Locate every uninfected red blood cell.
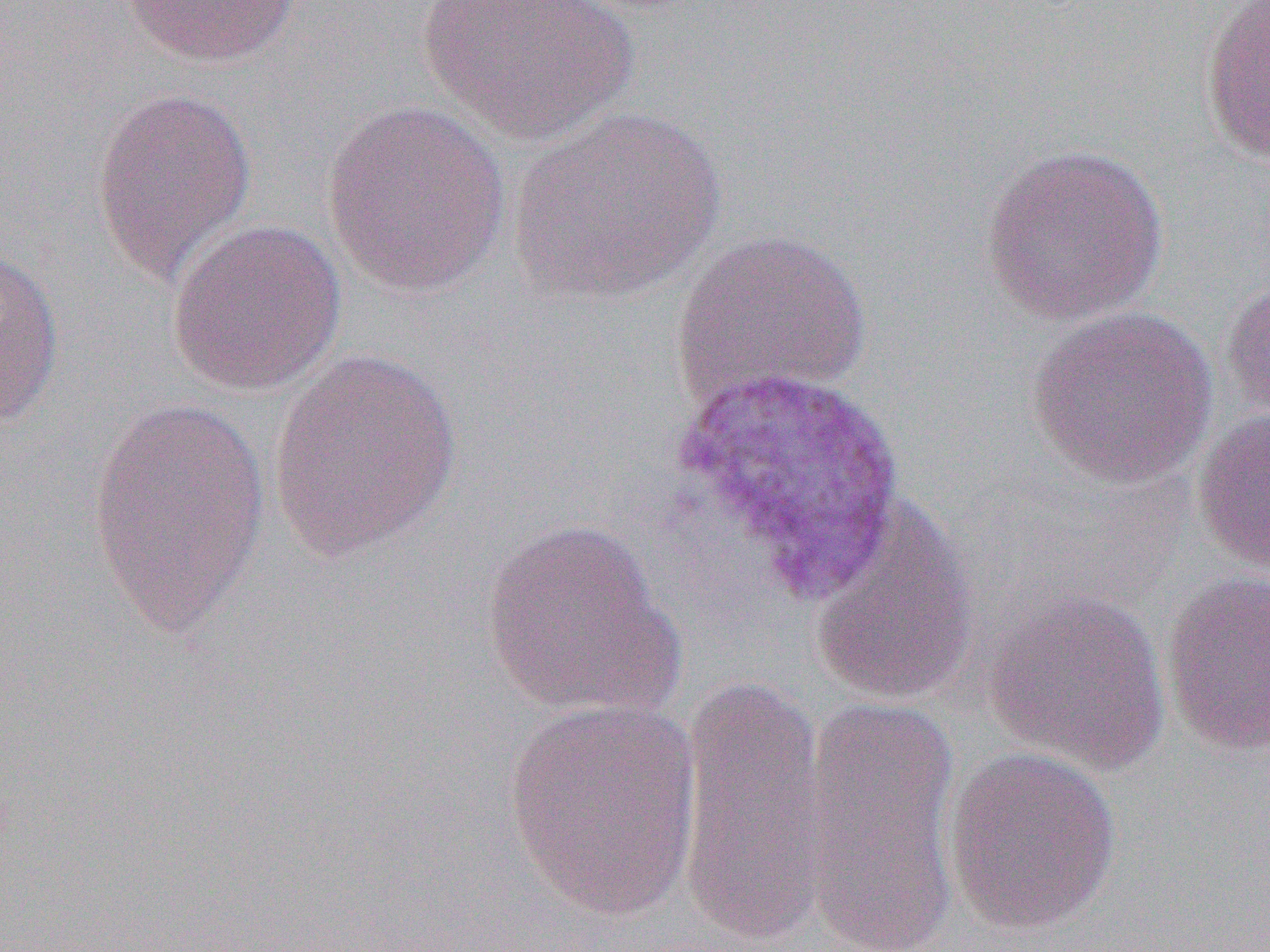

Approximate bounding boxes as (x1, y1, x2, y2) in pixels.
Uninfected red blood cells (subset): (118, 0, 302, 69), (417, 0, 638, 147), (1199, 1, 1269, 170), (91, 85, 257, 286), (320, 100, 513, 297), (509, 105, 725, 304), (979, 142, 1169, 326), (167, 218, 346, 396), (669, 227, 873, 412), (0, 246, 65, 431), (1221, 270, 1270, 424), (1026, 304, 1219, 489), (266, 347, 464, 564), (84, 393, 272, 643), (1191, 406, 1270, 574), (808, 494, 982, 706), (480, 518, 682, 721), (1160, 571, 1270, 758), (983, 587, 1172, 776), (675, 678, 834, 945), (797, 693, 962, 950), (501, 697, 703, 921), (942, 746, 1122, 937).

slide-level diagnosis = Plasmodium vivax
modality = optical microscopy
image size = 1270×952 pixels
field of view = one of a larger specimen
magnification = 1000x
preparation = thin blood smear